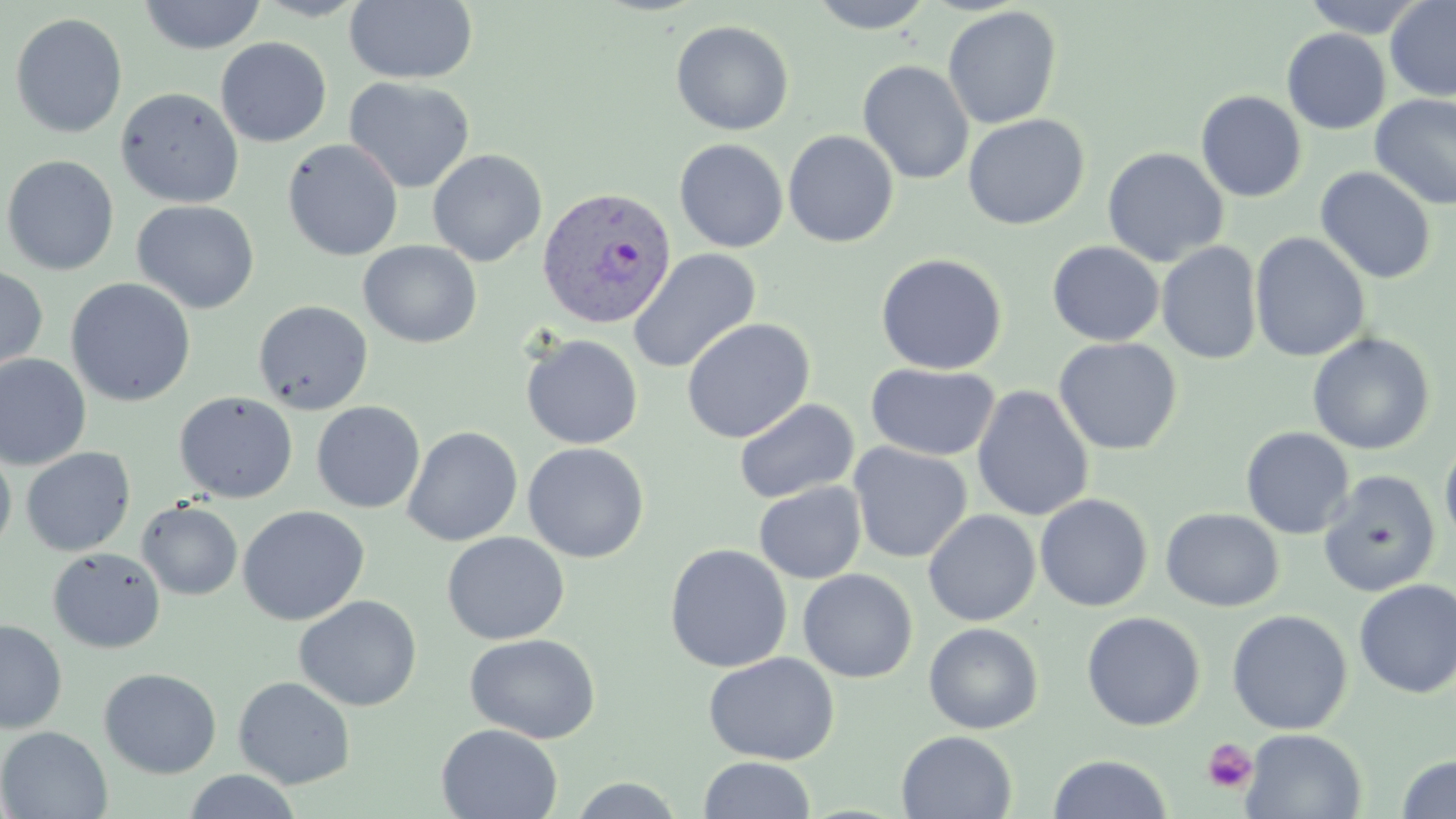
Summary:
  - Coordinate format: approximate bounding boxes as [x1, y1, x2, y2] in pixels
  - Platelet locations: [1202, 739, 1258, 794]
  - Uninfected red blood cell locations: [138, 0, 267, 54], [251, 0, 373, 21], [806, 0, 937, 34], [1301, 0, 1429, 38], [1385, 0, 1456, 101], [344, 1, 479, 85], [942, 6, 1062, 130], [10, 12, 128, 139], [670, 20, 794, 136], [1281, 28, 1390, 134], [215, 37, 332, 147], [857, 60, 974, 185], [344, 77, 475, 194], [115, 87, 244, 208], [1195, 91, 1307, 202], [1370, 93, 1456, 211], [962, 113, 1090, 230], [782, 130, 900, 248], [674, 138, 789, 252], [282, 139, 403, 261], [1102, 147, 1229, 267], [427, 149, 547, 266], [1, 154, 119, 276], [1315, 167, 1436, 284], [132, 200, 260, 314], [1250, 232, 1370, 363], [358, 240, 482, 348], [1046, 241, 1165, 346], [1156, 241, 1263, 365], [627, 248, 762, 374], [874, 253, 1009, 375], [0, 265, 49, 377], [65, 278, 196, 407], [253, 299, 373, 415], [681, 317, 815, 444], [1307, 332, 1435, 455], [521, 334, 644, 449], [1053, 337, 1183, 455], [0, 354, 91, 470], [865, 363, 1000, 461], [971, 384, 1095, 522], [175, 392, 298, 503], [734, 398, 859, 504], [311, 401, 425, 514], [402, 426, 523, 547], [1241, 426, 1354, 539], [1439, 436, 1456, 550], [522, 442, 649, 562], [848, 442, 972, 563], [0, 445, 17, 559], [20, 447, 136, 557], [1318, 470, 1441, 597], [754, 481, 866, 584], [1035, 493, 1154, 612], [137, 500, 243, 600], [237, 506, 369, 626], [1161, 507, 1284, 612], [923, 509, 1040, 627], [441, 531, 570, 645], [664, 543, 793, 673], [47, 547, 165, 653], [798, 568, 918, 683], [1354, 579, 1456, 699], [294, 595, 423, 711], [1226, 609, 1352, 735], [1081, 611, 1206, 731], [0, 620, 67, 734], [923, 622, 1044, 734], [464, 633, 601, 744], [703, 652, 840, 765], [98, 668, 222, 778], [233, 676, 356, 789], [436, 723, 562, 819], [0, 726, 112, 818], [1241, 728, 1367, 818], [896, 730, 1017, 818], [1047, 754, 1173, 819], [1396, 754, 1456, 818], [698, 756, 816, 818], [182, 770, 303, 819], [566, 776, 687, 818]
  - Plasmodium vivax-infected red blood cell locations: [537, 186, 677, 330]
  - Slide-level diagnosis: Plasmodium vivax
  - Modality: light microscopy
  - Field of view: one of a larger specimen
  - Preparation: thin blood smear
  - Magnification: 1000x
  - Stain: May-Grünwald-Giemsa
  - Image size: 1456×819 pixels